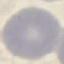

result = negative for malaria parasites
image type = cell patch, automatically extracted from a larger field of view and resized to 64 × 64 pixels
stain = Giemsa
preparation = thin blood smear
capture = smartphone camera at the microscope eyepiece